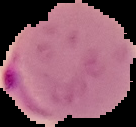
preparation = thin blood smear
image type = segmented cell region on a black background
image size = 136×127 pixels
result = malaria parasites identified